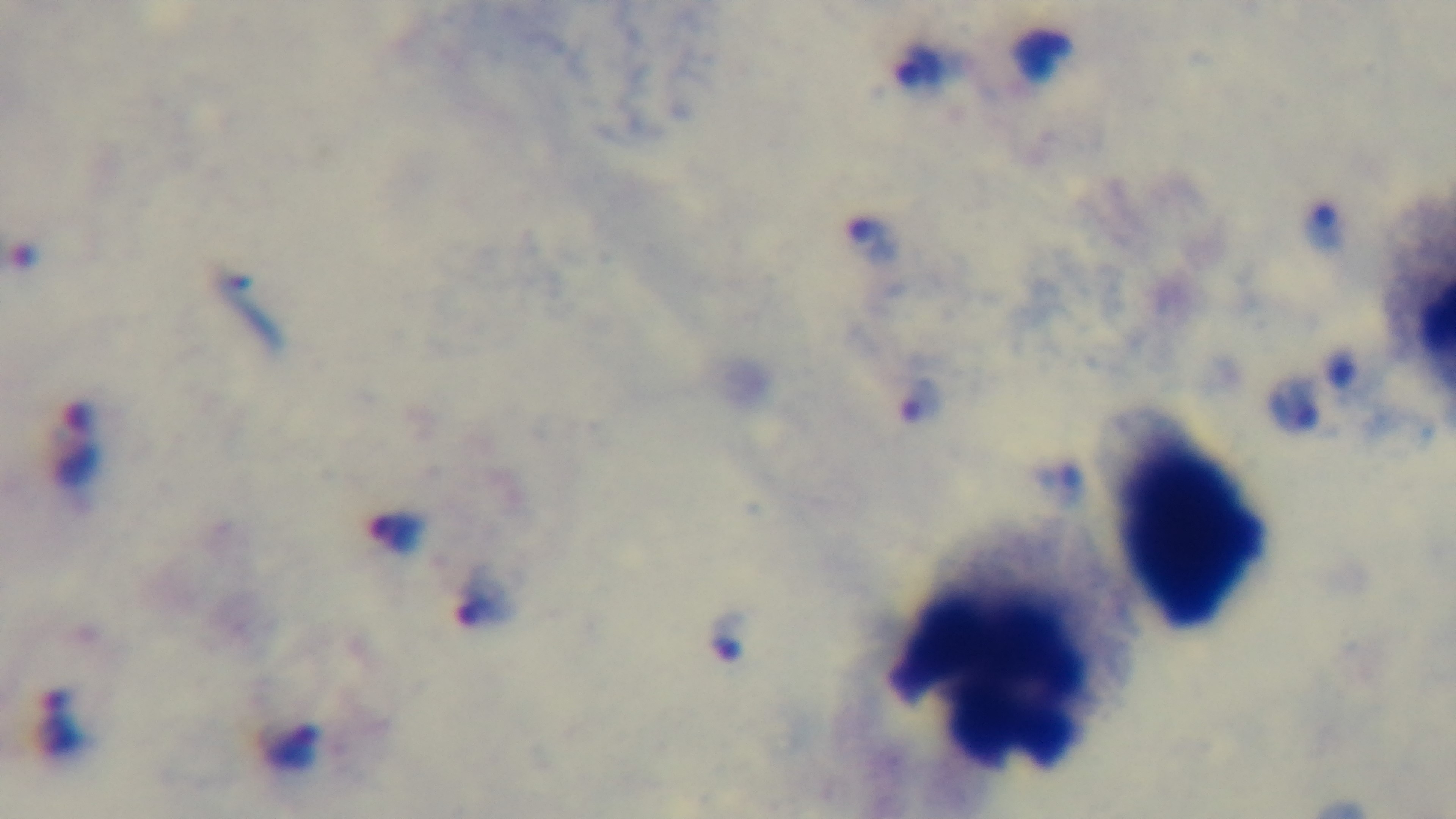

Preparation: thick blood film. Giemsa stain. 100x oil-immersion objective. Light microscopy. Malaria status: positive. Single field of view. Captured with a mounted 4K digital camera.